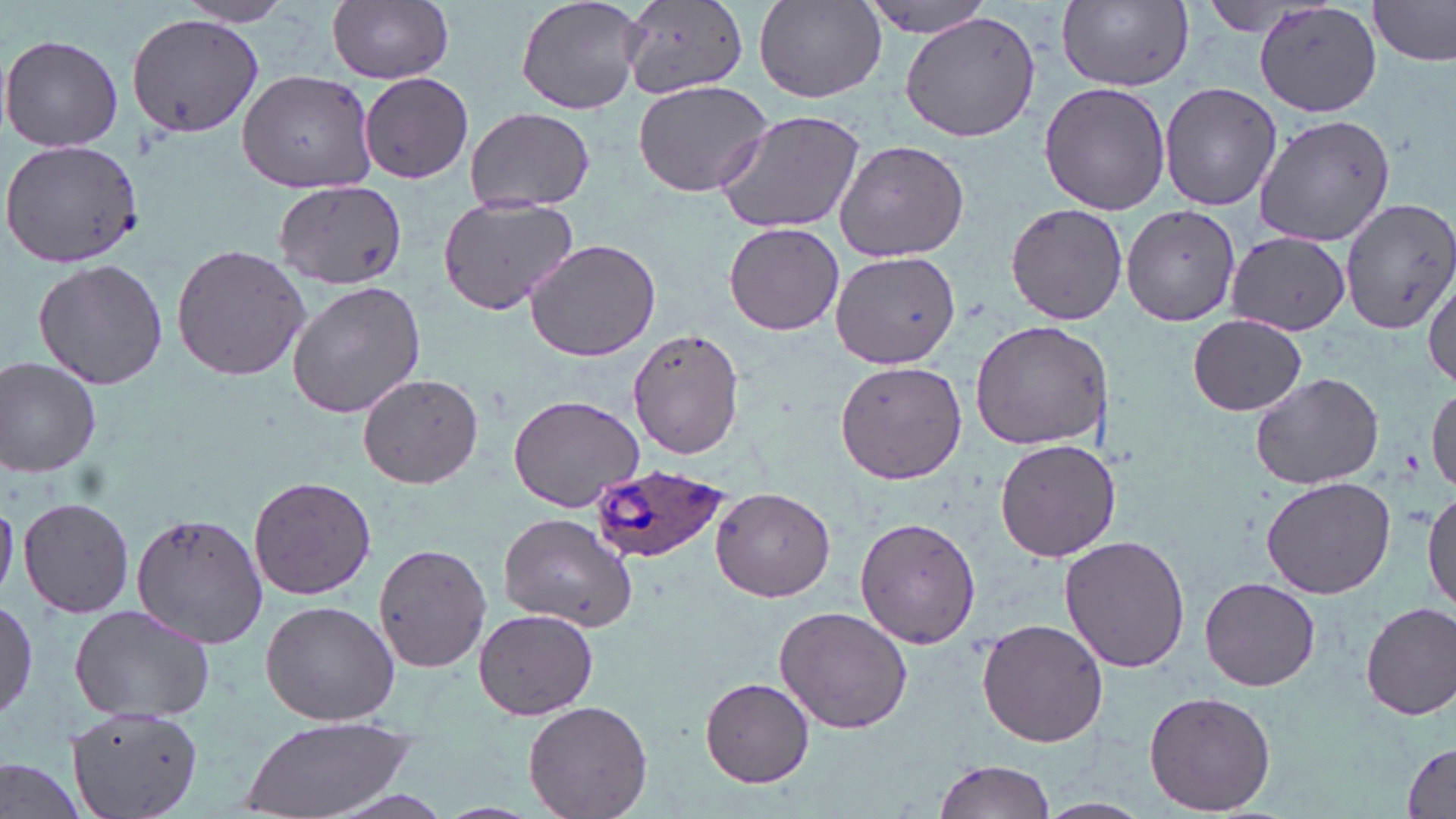 Approximate bounding boxes as [x1, y1, x2, y2] in pixels. Plasmodium ovale-infected red blood cell locations: [590, 465, 730, 562]. Uninfected red blood cell locations: [326, 0, 455, 84], [515, 0, 645, 116], [855, 0, 1002, 38], [1056, 0, 1194, 89], [176, 1, 296, 28], [621, 1, 749, 100], [755, 1, 884, 103], [1256, 1, 1383, 117], [1370, 2, 1455, 67], [898, 10, 1044, 142], [126, 12, 263, 137], [2, 33, 124, 152], [237, 68, 377, 193], [359, 70, 474, 183], [632, 80, 773, 197], [1039, 81, 1172, 214], [1161, 81, 1283, 212], [464, 106, 596, 211], [713, 108, 867, 235], [1255, 113, 1395, 246], [3, 137, 146, 270], [833, 137, 972, 262], [273, 180, 409, 290], [436, 193, 582, 316], [1342, 200, 1456, 337], [1005, 203, 1129, 324], [1120, 207, 1241, 326], [724, 221, 845, 337], [1225, 231, 1350, 335], [524, 239, 661, 361], [171, 242, 312, 382], [830, 249, 963, 368], [33, 256, 169, 391], [1424, 268, 1456, 388], [287, 277, 426, 419], [1187, 313, 1308, 416], [971, 319, 1112, 451], [630, 329, 746, 460], [1, 358, 103, 479], [836, 360, 967, 483], [1249, 371, 1386, 492], [357, 372, 485, 491], [1428, 382, 1456, 492], [506, 393, 646, 513], [995, 438, 1120, 563], [248, 475, 377, 601], [1262, 476, 1396, 600], [1424, 485, 1456, 617], [711, 486, 835, 602], [18, 496, 135, 619], [0, 499, 18, 600], [134, 508, 269, 649], [499, 511, 638, 631], [855, 517, 981, 648], [1060, 535, 1190, 673], [373, 540, 491, 675], [1202, 577, 1321, 691], [0, 596, 37, 726], [259, 600, 401, 726], [1359, 601, 1455, 719], [775, 603, 915, 734], [66, 605, 220, 722], [474, 609, 598, 719], [978, 616, 1109, 749], [700, 677, 815, 788], [1143, 690, 1276, 815], [522, 699, 654, 819], [67, 705, 204, 819], [239, 715, 416, 819], [1401, 743, 1456, 818], [0, 757, 90, 819], [930, 758, 1058, 818], [1035, 797, 1149, 819]. Slide-level diagnosis: Plasmodium ovale. Image is 1456×819 pixels. Single field of view. Light microscopy. Captured at 1000x magnification. Thin blood smear. May-Grünwald-Giemsa stain.